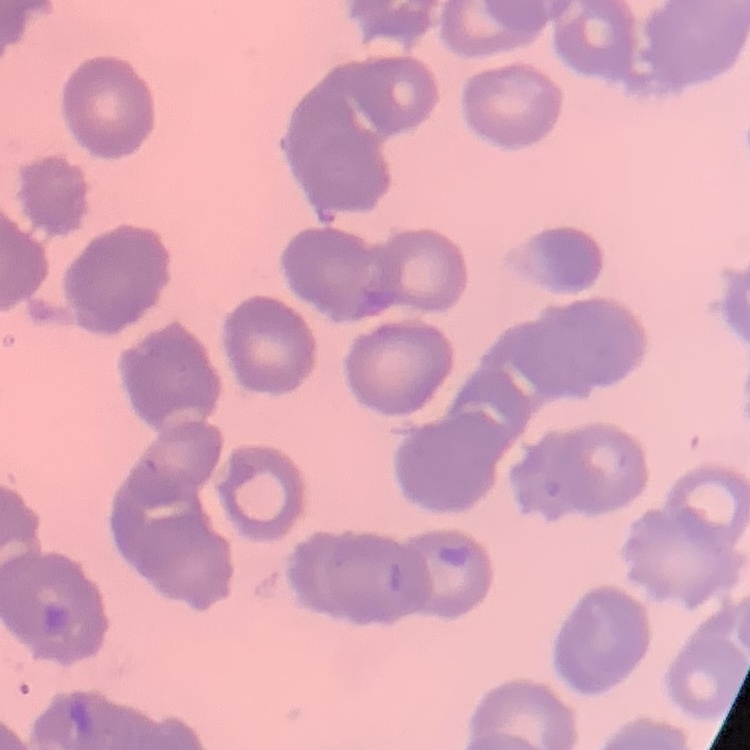

red blood cell morphology = rouleaux formation
image type = one tile cut from a larger photomicrograph
preparation = thin blood film
stain = Field's or Giemsa